Locate every blood parasite and identify its species.
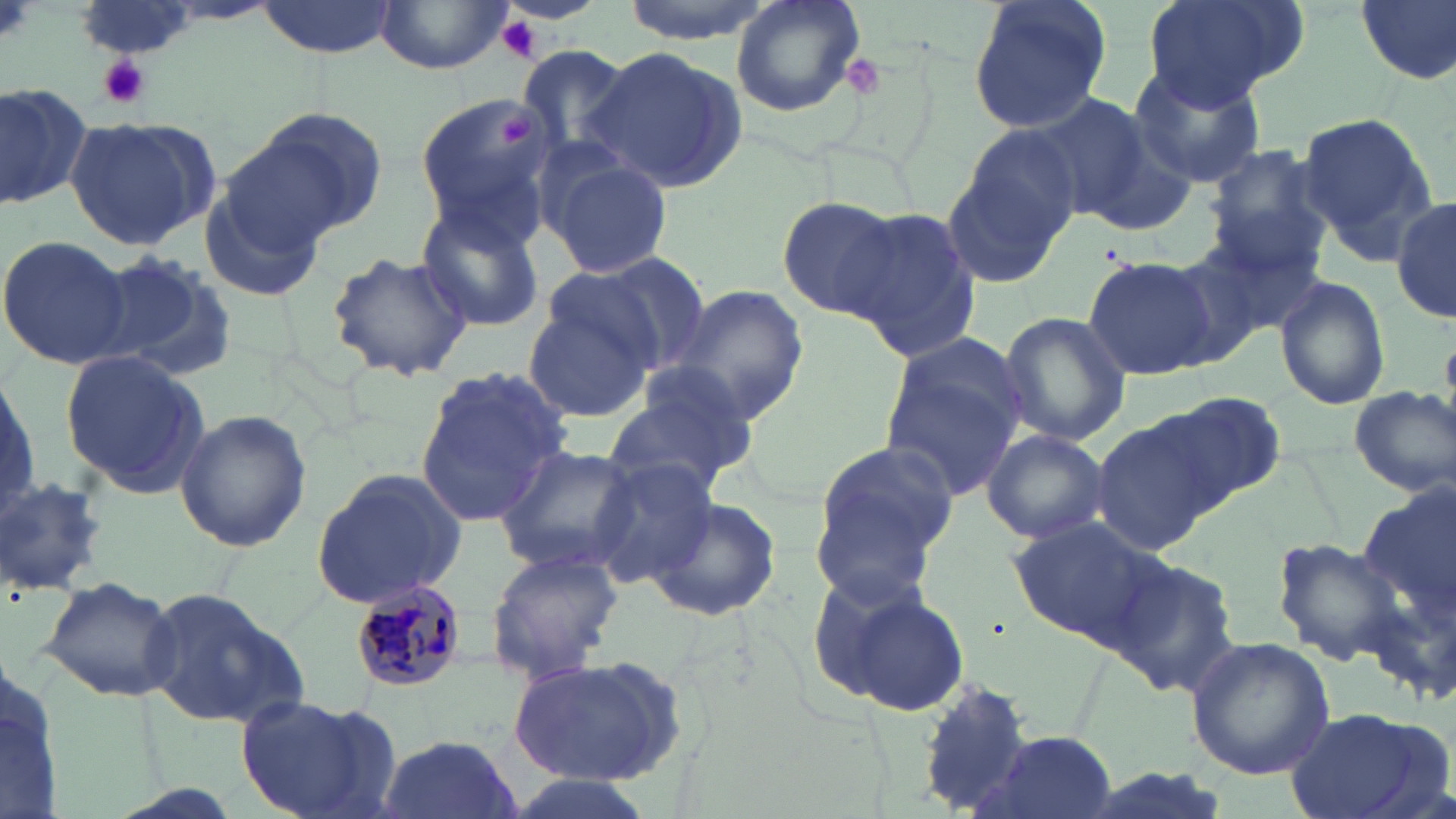

Approximate bounding boxes as (x1, y1, x2, y2) in pixels.
Plasmodium malariae-infected red blood cells: (347, 577, 473, 694).
No Plasmodium falciparum, Plasmodium ovale, Plasmodium vivax, Babesia divergens, or Trypanosoma brucei observed.

Platelet locations: (0, 0, 33, 48), (497, 16, 543, 62), (835, 53, 888, 102), (98, 55, 152, 108), (497, 111, 540, 149). Uninfected red blood cell locations: (254, 0, 400, 60), (618, 0, 777, 42), (730, 0, 865, 119), (966, 0, 1114, 134), (1140, 0, 1305, 110), (1355, 0, 1456, 86), (373, 2, 513, 73), (516, 43, 635, 157), (584, 46, 748, 192), (1125, 62, 1269, 188), (0, 78, 91, 209), (412, 92, 560, 236), (1036, 93, 1186, 230), (237, 107, 387, 243), (1297, 112, 1433, 249), (62, 118, 220, 251), (942, 130, 1079, 288), (1201, 147, 1333, 274), (543, 154, 672, 278), (200, 174, 332, 303), (1392, 196, 1455, 322), (777, 197, 906, 322), (413, 202, 545, 332), (847, 209, 983, 363), (1189, 223, 1326, 341), (0, 235, 130, 368), (1157, 247, 1275, 371), (326, 250, 474, 383), (91, 251, 236, 380), (561, 253, 709, 372), (1082, 255, 1217, 382), (1275, 277, 1391, 412), (665, 283, 810, 424), (523, 297, 657, 422), (997, 311, 1130, 444), (877, 342, 1029, 502), (60, 351, 210, 497), (414, 368, 573, 525), (602, 374, 758, 498), (1349, 387, 1455, 498), (1162, 394, 1287, 508), (175, 409, 313, 551), (1092, 417, 1219, 557), (981, 427, 1109, 545), (809, 438, 958, 581), (491, 444, 642, 575), (1, 457, 109, 606), (583, 463, 720, 587), (310, 468, 471, 610), (647, 495, 782, 622), (1011, 519, 1160, 643), (1272, 537, 1411, 665), (485, 548, 624, 683), (1104, 557, 1242, 694), (40, 576, 180, 701), (816, 579, 970, 717), (143, 590, 312, 727), (1185, 638, 1335, 779), (0, 642, 67, 819), (508, 657, 691, 785), (915, 680, 1033, 813), (236, 692, 397, 819), (1281, 707, 1449, 819), (973, 731, 1121, 818), (374, 732, 520, 819). Slide-level diagnosis: Plasmodium malariae. Thin blood film. One field of a larger specimen. Image is 1456×819 pixels. 1000x magnification. May-Grünwald-Giemsa-stained preparation. Light microscopy.